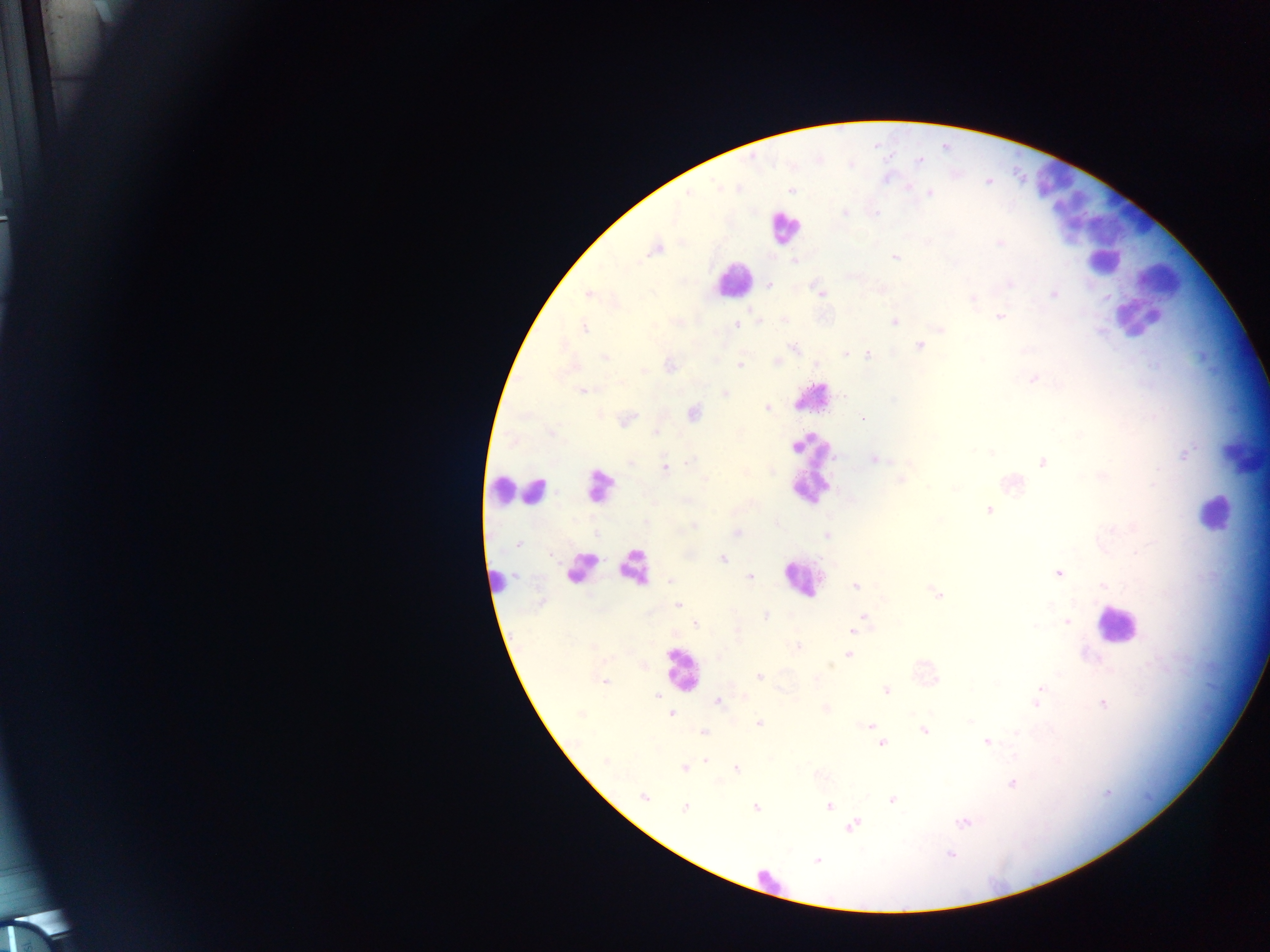
Approximate centers as [x, y] in pixels. Plasmodium parasite locations: [905, 186], [791, 190], [686, 192], [929, 194], [844, 212], [1000, 243], [656, 248], [894, 257], [795, 260], [1009, 283], [769, 284], [588, 294], [823, 294], [1053, 294], [972, 298], [999, 316], [782, 319], [893, 321], [736, 323], [584, 327], [940, 329], [919, 345], [793, 347], [844, 353], [868, 355], [605, 357], [775, 362], [739, 364], [668, 366], [1034, 377], [582, 390], [724, 392], [766, 407], [693, 413], [862, 417], [625, 420], [1186, 452], [874, 458], [1043, 463], [664, 467], [1102, 474], [900, 480], [1010, 482], [990, 510], [694, 527], [736, 534], [827, 535], [518, 544], [723, 559], [1058, 573], [749, 576], [669, 581], [1101, 583], [856, 585], [938, 594], [678, 605], [765, 615], [864, 617], [695, 623], [1067, 623], [853, 631], [797, 647], [849, 653], [759, 677], [604, 680], [1041, 687], [886, 691], [657, 695], [717, 701], [1037, 703], [1102, 704], [825, 708], [670, 713], [758, 723], [869, 725], [924, 730], [703, 733], [986, 741], [881, 743], [706, 760], [685, 767], [735, 768], [1012, 782], [644, 797], [892, 799], [828, 805], [756, 806], [685, 807], [963, 821], [852, 825], [949, 853], [817, 860]. Leukocyte locations: [1059, 181], [1129, 210], [1080, 220], [784, 227], [1103, 262], [1160, 279], [733, 280], [1137, 319], [813, 397], [1245, 456], [808, 465], [599, 486], [501, 489], [521, 491], [1215, 514], [633, 566], [581, 567], [802, 578], [496, 581], [1117, 624], [682, 670], [769, 882]. Mobile-phone photograph taken through the microscope. One field of view. Sample from Ghana. Image is 1270×952 pixels. Thick blood smear.